Outline each uninfected red blood cell.
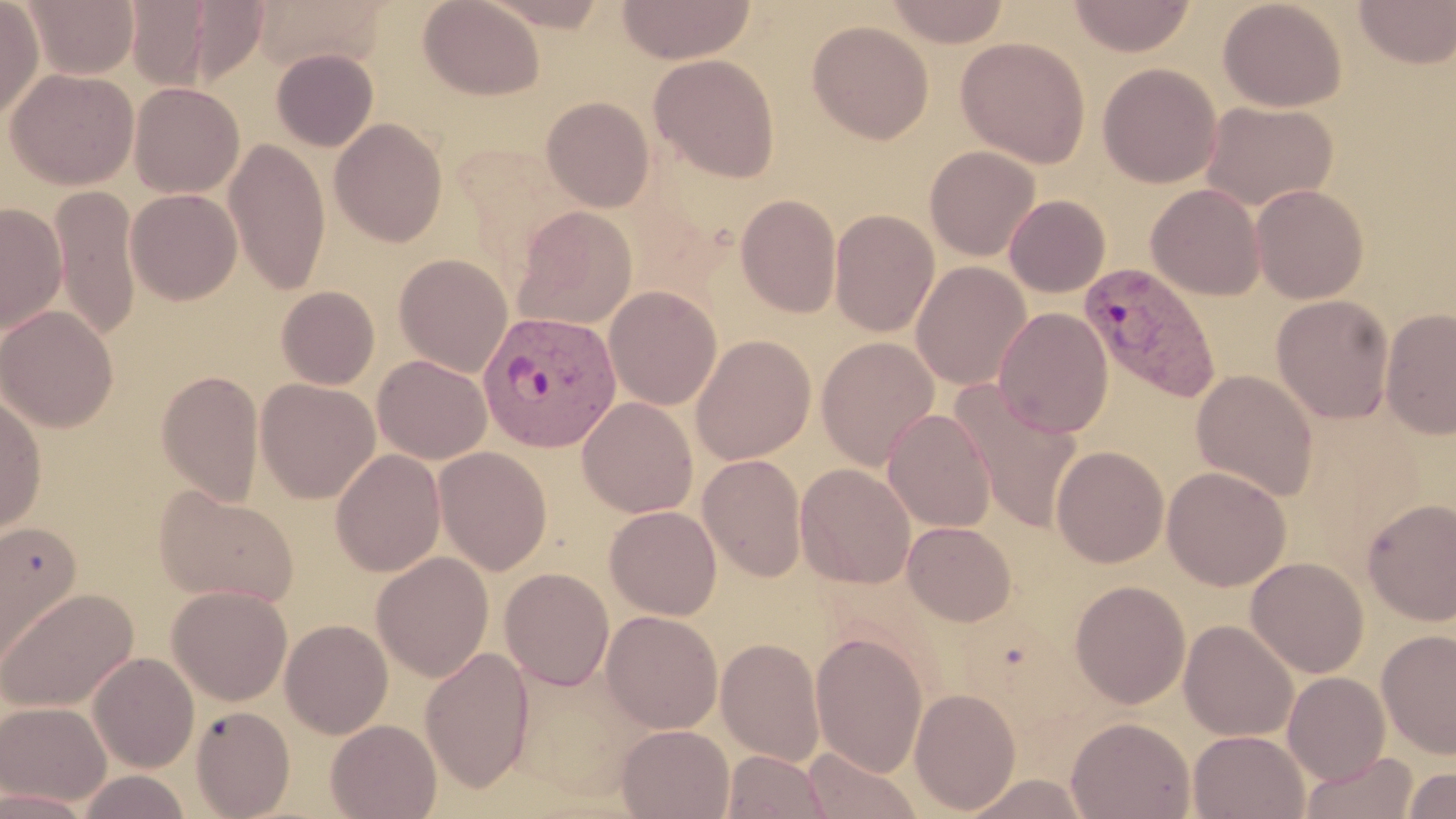

Approximate bounding boxes as (x1, y1, x2, y2) in pixels.
Uninfected red blood cells: (0, 0, 44, 122), (23, 0, 139, 79), (125, 0, 213, 90), (418, 0, 545, 100), (477, 0, 614, 31), (617, 0, 757, 64), (884, 0, 1011, 47), (1068, 0, 1196, 56), (1217, 0, 1347, 112), (179, 1, 270, 86), (250, 1, 386, 71), (1353, 1, 1456, 69), (807, 20, 934, 144), (955, 36, 1091, 168), (271, 48, 379, 151), (649, 54, 780, 182), (1098, 63, 1222, 188), (5, 67, 138, 189), (129, 81, 244, 198), (541, 96, 655, 212), (1201, 100, 1338, 211), (329, 118, 448, 247), (225, 137, 330, 295), (924, 145, 1041, 261), (1146, 183, 1266, 300), (1250, 183, 1369, 304), (49, 187, 142, 343), (125, 188, 242, 305), (735, 193, 842, 318), (1004, 194, 1110, 297), (0, 202, 67, 334), (513, 205, 638, 330), (829, 208, 940, 337), (394, 253, 513, 377), (911, 261, 1032, 391), (277, 286, 380, 389), (604, 286, 722, 410), (1272, 295, 1394, 424), (1, 305, 118, 433), (993, 306, 1113, 438), (1380, 307, 1456, 439), (690, 334, 816, 465), (816, 337, 939, 470), (373, 355, 492, 464), (156, 369, 264, 505), (1192, 370, 1319, 501), (255, 378, 380, 503), (949, 381, 1084, 534), (0, 390, 47, 539), (577, 396, 698, 518), (883, 408, 997, 532), (1050, 445, 1168, 568), (433, 446, 553, 576), (331, 448, 446, 578), (698, 453, 807, 582), (795, 463, 916, 588), (1162, 465, 1291, 591), (154, 486, 299, 607), (1362, 497, 1456, 625), (605, 505, 722, 620), (1, 520, 81, 672), (902, 521, 1016, 626), (372, 551, 494, 681), (1245, 556, 1369, 678), (499, 568, 614, 691), (1069, 580, 1191, 709), (167, 585, 293, 705), (0, 587, 138, 712), (601, 610, 723, 733), (280, 618, 393, 739), (1179, 619, 1299, 741), (1376, 629, 1456, 759), (810, 630, 928, 778), (716, 637, 825, 765), (421, 647, 534, 791), (88, 652, 199, 772), (1283, 671, 1391, 784), (909, 687, 1021, 813), (0, 701, 111, 806), (190, 705, 295, 818), (1066, 716, 1195, 819), (326, 718, 442, 819), (617, 724, 735, 818), (1188, 730, 1309, 818), (802, 747, 922, 819), (722, 750, 832, 819), (1301, 751, 1417, 818), (1402, 766, 1456, 818), (77, 770, 194, 818), (962, 773, 1092, 818).

Plasmodium vivax-infected red blood cell locations: (1078, 262, 1223, 404), (479, 310, 621, 453). Slide-level diagnosis: Plasmodium vivax. Light microscopy. Image is 1456×819 pixels. One field of a larger specimen. Thin blood smear. 1000x magnification. May-Grünwald-Giemsa-stained preparation.